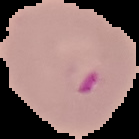

preparation = thin blood smear
result = malaria parasites identified
image type = segmented cell region with the area outside set to black
image size = 139×139 pixels